Report the malaria status of this cell.
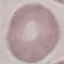
Uninfected.

{
  "capture": "smartphone through the microscope eyepiece",
  "stain": "Giemsa",
  "image_type": "cell patch, automatically extracted from a larger field of view and resized to 64 × 64 pixels",
  "preparation": "thin blood film"
}